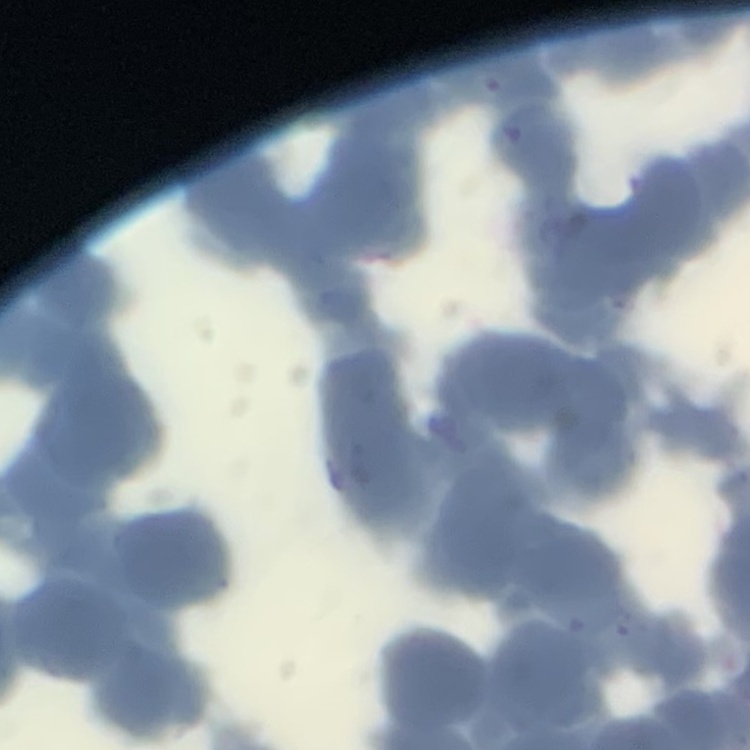 The red blood cells exhibit rouleaux formation. Thin blood film. Field's or Giemsa stain. Square crop of a larger photomicrograph.